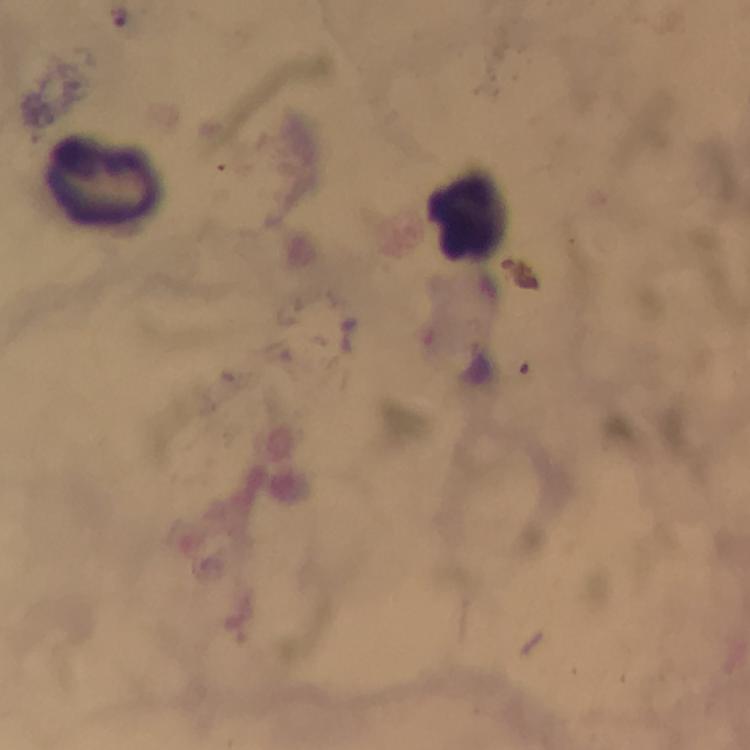
Approximate object centers, in pixels from the top-left corner.
Summary:
  - Leukocyte locations: (x=106, y=183), (x=473, y=218)
  - Plasmodium parasite locations: (x=118, y=15)
  - Cropped from: a single field of view
  - Stain: Giemsa
  - Image size: 750×750 pixels
  - Context: from a malaria diagnostic workup
  - Capture: smartphone camera through the microscope
  - Immersion oil: used
  - Magnification: 100x
  - Preparation: thick smear